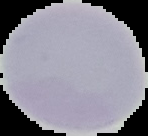
Summary:
  - Malaria status: uninfected
  - Image type: cell region segmented out of the field of view; surrounding area masked to black
  - Preparation: thin blood film
  - Image size: 148×136 pixels